Report the malaria status of this cell.
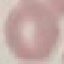

It is uninfected.

Acquired by smartphone through the microscope eyepiece. Thin smear of blood. Giemsa stain. Automatically extracted cell patch, resized to 64 × 64 pixels.